Classify this cell by malaria status.
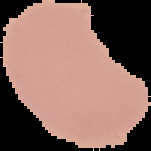
Uninfected.

preparation: thin blood film
image_type: cell region segmented out of the field of view; surrounding area masked to black
image_size: 151×151 pixels